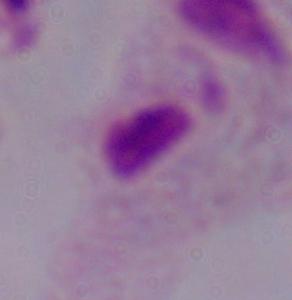

identification = trichomonad
magnification = 1000x
modality = micrograph